Outline each blood parasite and name the species.
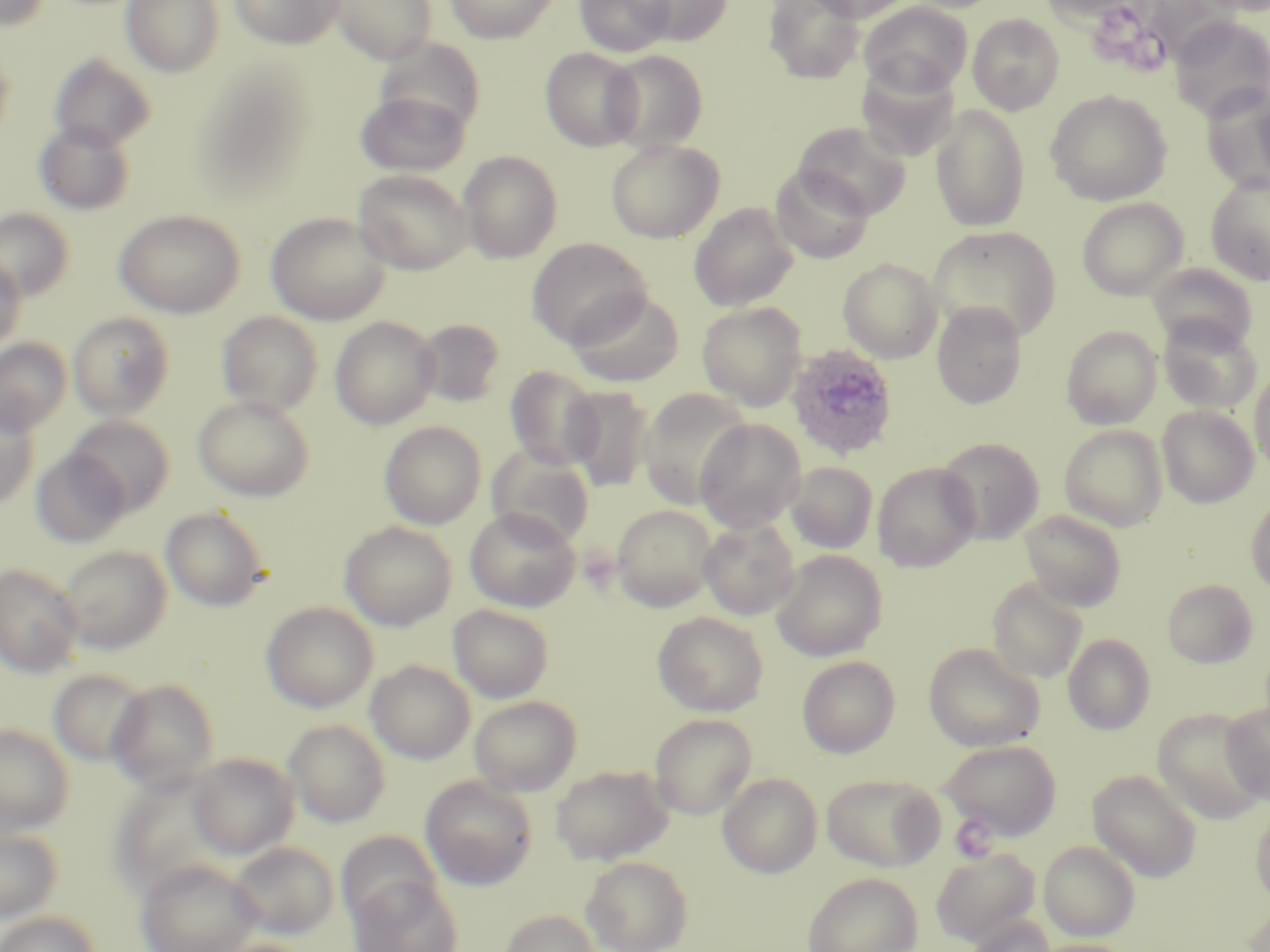
Approximate bounding boxes as (x1, y1, x2, y2) in pixels.
Plasmodium ovale-infected red blood cells: (785, 343, 899, 461).
No Plasmodium falciparum, Plasmodium malariae, Plasmodium vivax, Babesia divergens, or Trypanosoma brucei observed.

Uninfected red blood cell locations: (0, 0, 51, 32), (121, 0, 225, 77), (229, 0, 343, 49), (331, 0, 438, 64), (443, 0, 560, 43), (574, 0, 676, 57), (632, 0, 732, 46), (763, 0, 865, 84), (802, 0, 921, 23), (1037, 0, 1146, 26), (1192, 0, 1270, 17), (859, 1, 973, 97), (967, 14, 1064, 115), (1170, 15, 1270, 122), (0, 43, 14, 144), (541, 47, 644, 151), (602, 50, 708, 151), (49, 53, 156, 152), (856, 63, 960, 164), (1201, 85, 1270, 196), (355, 90, 470, 177), (1045, 90, 1172, 206), (930, 103, 1030, 232), (33, 121, 135, 216), (794, 121, 912, 220), (606, 139, 724, 243), (458, 150, 563, 263), (770, 165, 873, 264), (353, 169, 473, 274), (1205, 173, 1270, 286), (1078, 198, 1188, 300), (689, 203, 798, 311), (0, 208, 75, 302), (113, 210, 245, 318), (265, 212, 391, 325), (927, 226, 1063, 343), (527, 237, 652, 348), (0, 253, 26, 353), (838, 257, 943, 363), (1147, 262, 1256, 351), (565, 289, 685, 387), (697, 301, 807, 410), (931, 302, 1027, 409), (216, 311, 323, 417), (68, 312, 175, 419), (1157, 314, 1261, 414), (330, 316, 440, 430), (414, 318, 506, 407), (1061, 324, 1162, 430), (0, 337, 71, 436), (1250, 364, 1270, 476), (505, 366, 601, 471), (564, 386, 655, 492), (638, 387, 753, 510), (192, 395, 315, 502), (0, 401, 40, 508), (1158, 405, 1258, 508), (65, 415, 175, 515), (695, 418, 806, 533), (379, 420, 487, 529), (1060, 424, 1168, 531), (936, 438, 1044, 545), (487, 447, 595, 548), (31, 449, 130, 548), (786, 462, 878, 554), (873, 462, 980, 572), (1246, 494, 1270, 596), (611, 504, 718, 611), (160, 506, 271, 612), (464, 506, 581, 612), (1019, 509, 1127, 611), (698, 518, 800, 620), (339, 521, 457, 630), (59, 545, 172, 654), (791, 549, 894, 757), (771, 550, 887, 661), (0, 563, 84, 678), (987, 577, 1088, 683), (1162, 579, 1258, 668), (261, 601, 378, 713), (448, 604, 554, 702), (653, 611, 768, 716), (1063, 633, 1155, 734), (923, 642, 1045, 752), (797, 656, 900, 758), (366, 660, 475, 764), (48, 669, 150, 766), (107, 678, 221, 792), (469, 695, 581, 796), (1220, 702, 1270, 804), (1153, 708, 1266, 823), (649, 713, 757, 820), (283, 719, 390, 827), (0, 724, 74, 837), (940, 739, 1062, 840), (188, 752, 299, 859), (550, 765, 674, 865), (1086, 770, 1202, 882), (718, 772, 822, 878), (822, 773, 945, 872), (420, 776, 538, 890), (1250, 804, 1270, 908), (0, 824, 62, 924), (336, 831, 442, 927), (1039, 840, 1141, 941), (229, 841, 337, 939), (931, 848, 1040, 948), (581, 854, 693, 952), (134, 859, 264, 952), (802, 872, 923, 952), (349, 877, 463, 952), (1241, 902, 1270, 952), (498, 909, 602, 952), (0, 911, 100, 952), (967, 915, 1056, 952), (209, 937, 317, 952), (1030, 938, 1135, 952). Platelet locations: (949, 815, 998, 863). Slide-level diagnosis: Plasmodium ovale. May-Grünwald-Giemsa-stained preparation. Thin blood smear. 1000x magnification. Image is 1270×952 pixels. Single field of view. Optical microscopy.